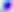
{
  "identification": "Toxoplasma gondii",
  "magnification": "400x",
  "modality": "micrograph"
}